Report the malaria status of this cell.
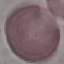
It is uninfected.

Photographed with a smartphone camera at the microscope eyepiece. Cell patch, automatically extracted from a larger field of view and resized to 64 × 64 pixels. Giemsa stain. Thin smear of blood.